Assess this cell for malaria.
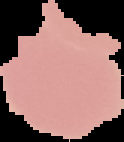

Uninfected.

Segmented cell region on a black background. Image is 124×142 pixels. From a thin blood smear.